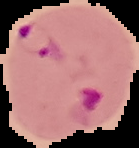

image_type: cell region segmented out of the field of view; surrounding area masked to black
image_size: 139×148 pixels
preparation: thin blood smear
result: malaria parasites detected